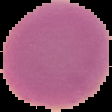
Summary:
  - Malaria status: uninfected
  - Image type: segmented cell region with the area outside set to black
  - Image size: 112×112 pixels
  - Preparation: thin blood smear